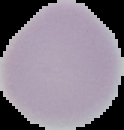

Summary:
  - Image size: 124×130 pixels
  - Result: no Plasmodium parasites seen
  - Preparation: thin blood film
  - Image type: segmented cell region on a black background